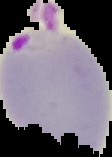

image type = segmented cell region with the area outside set to black
image size = 112×157 pixels
preparation = thin blood film
result = Plasmodium parasites identified